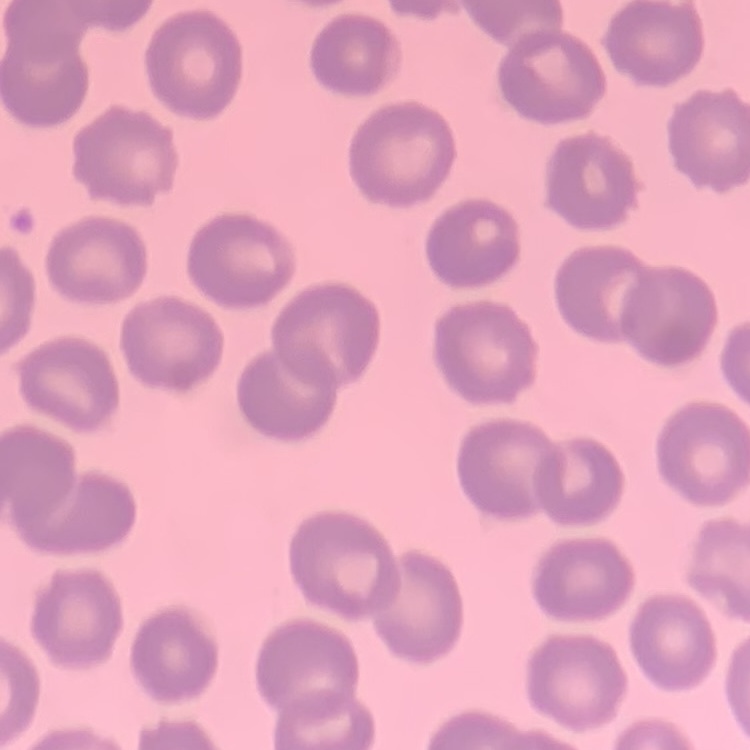

Summary:
  - Erythrocyte morphology: no rouleaux formation
  - Stain: Field's or Giemsa
  - Preparation: thin blood film
  - Image type: one tile cut from a larger photomicrograph